Identify the preparation type.
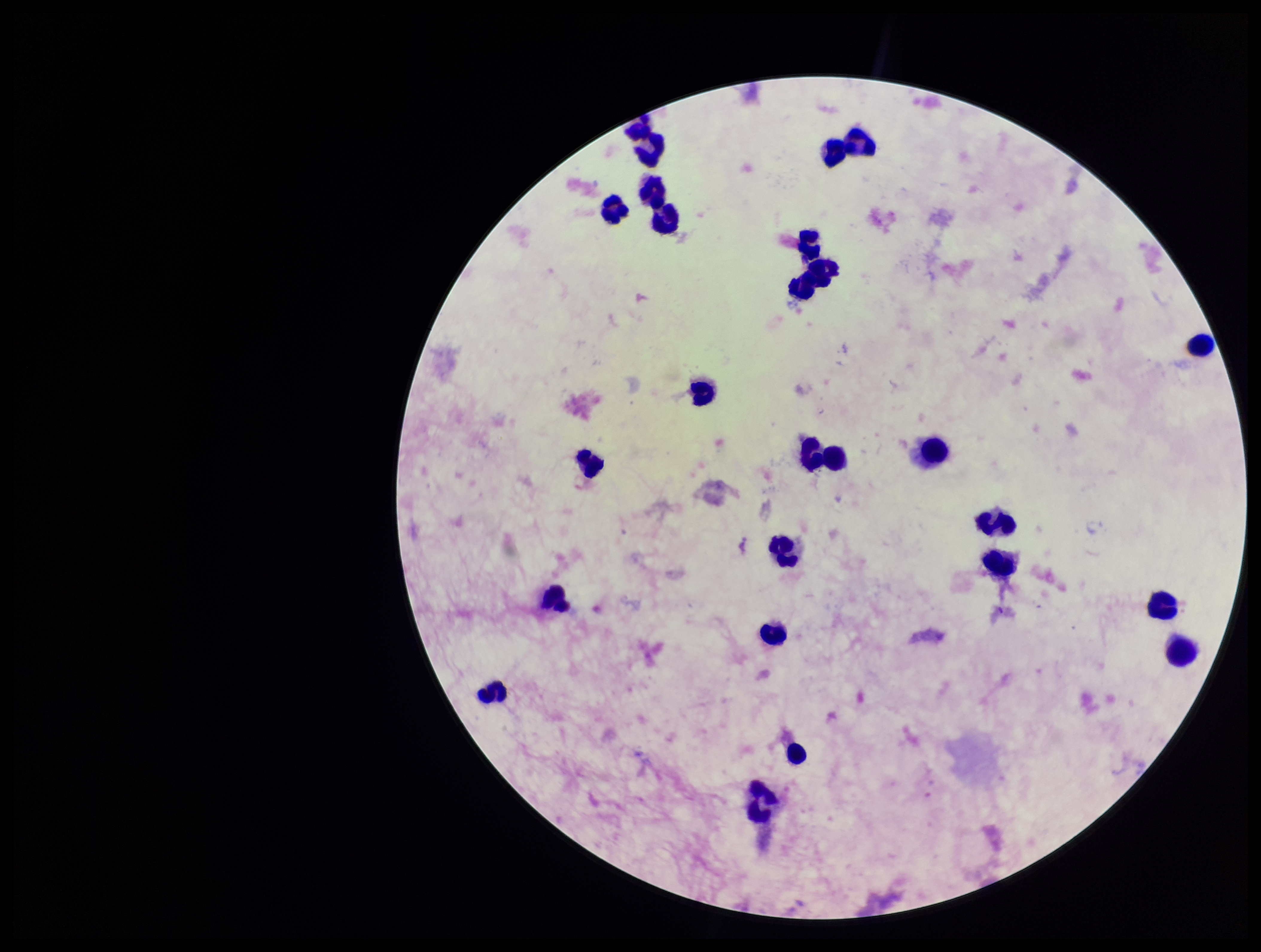
It is a thick blood smear.

leukocyte_count: 22
patient_malaria_status: positive
parasite_count: 0
capture: smartphone photograph through the microscope eyepiece
plasmodium_parasites: none identified
field_of_view: single
stain: Giemsa
species_reported_for_this_patient: Plasmodium vivax
image_size: 1261×952 pixels